Locate every Plasmodium parasite.
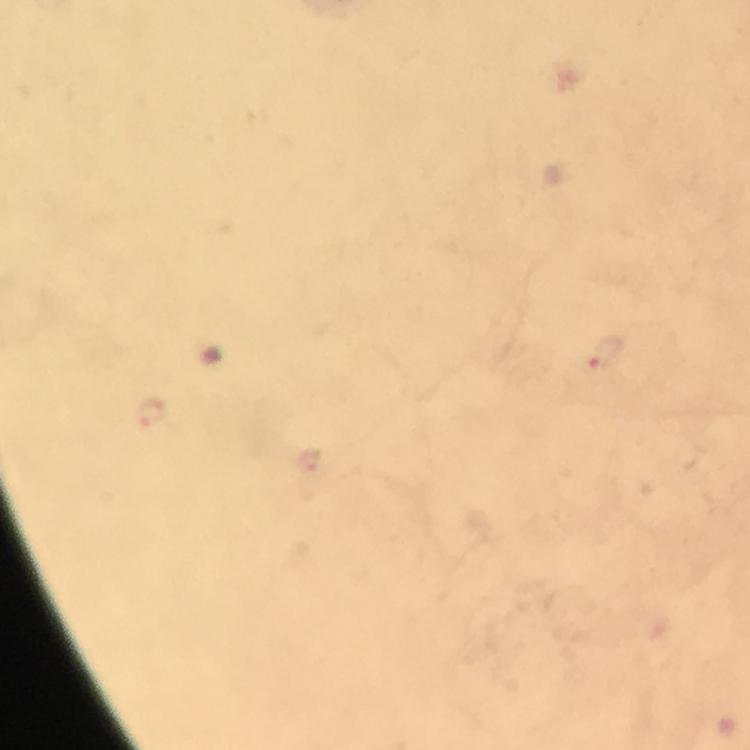

Approximate object centers, in pixels from the top-left corner.
Plasmodium parasites: (x=606, y=355), (x=149, y=412), (x=308, y=460).

Summary:
  - Image size: 750×750 pixels
  - Preparation: thick smear
  - Immersion oil: used
  - Capture: smartphone mounted on the microscope
  - Cropped from: one field of view
  - Magnification: 100x
  - Stain: Giemsa
  - Context: from a diagnostic examination for malaria